Report the malaria status of this cell.
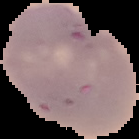
Uninfected.

image type = segmented cell region on a black background
preparation = thin blood smear
image size = 139×139 pixels